Identify the parasite.
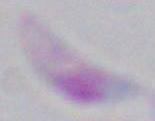
This is Toxoplasma gondii.

modality = micrograph
magnification = 1000x